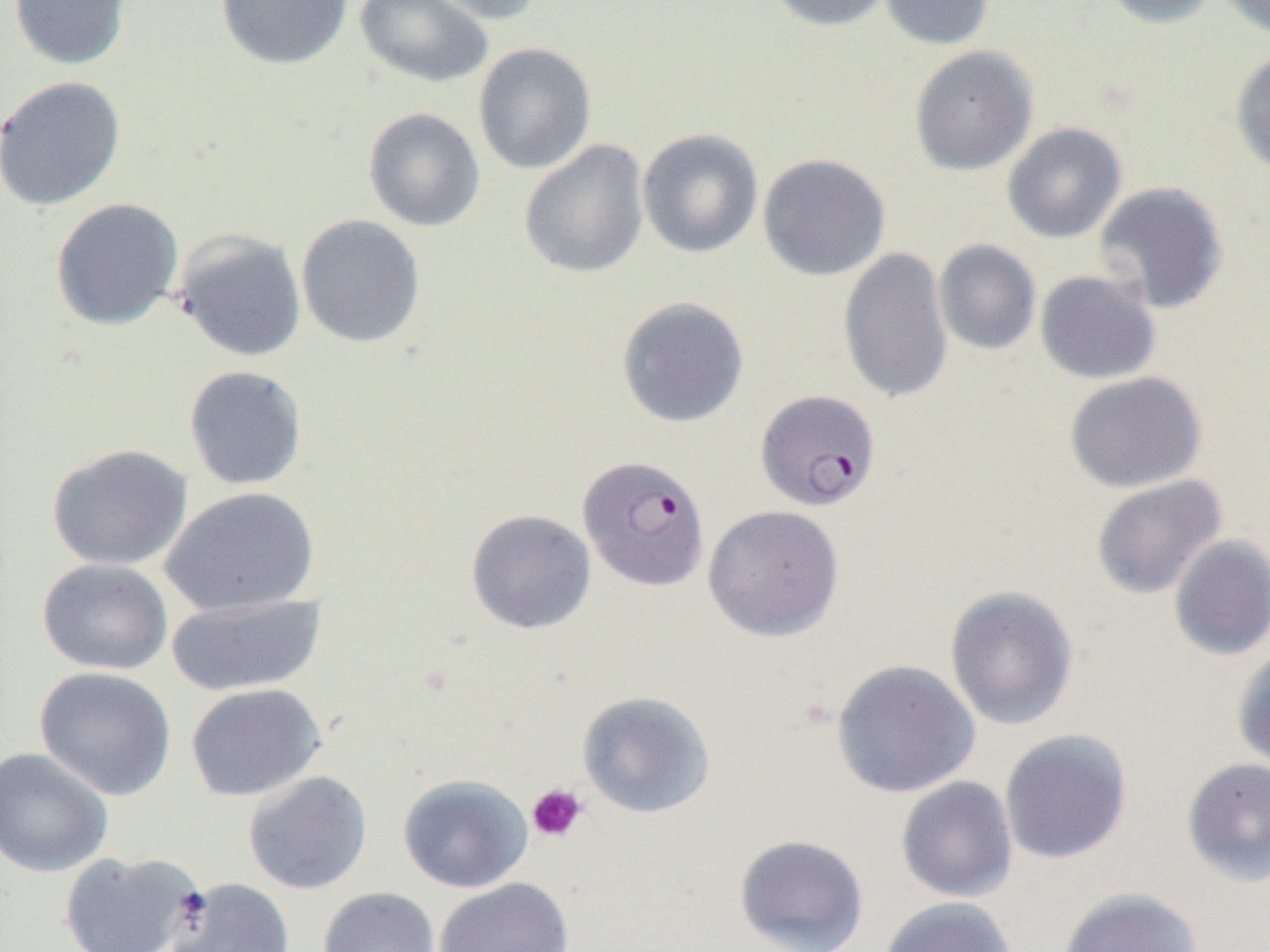

Approximate bounding boxes as named x1/y1/x2/y2 corners in pixels. Platelet locations: (x1=526, y1=784, x2=587, y2=842). Plasmodium falciparum-infected red blood cell locations: (x1=757, y1=391, x2=882, y2=513), (x1=577, y1=454, x2=711, y2=591). Uninfected red blood cell locations: (x1=7, y1=0, x2=132, y2=71), (x1=215, y1=0, x2=353, y2=70), (x1=354, y1=0, x2=494, y2=88), (x1=416, y1=0, x2=544, y2=25), (x1=766, y1=0, x2=895, y2=32), (x1=879, y1=0, x2=995, y2=50), (x1=1099, y1=0, x2=1223, y2=29), (x1=1216, y1=0, x2=1270, y2=38), (x1=473, y1=42, x2=597, y2=175), (x1=909, y1=45, x2=1038, y2=176), (x1=1230, y1=47, x2=1270, y2=180), (x1=0, y1=75, x2=126, y2=212), (x1=362, y1=107, x2=485, y2=233), (x1=1002, y1=122, x2=1126, y2=244), (x1=637, y1=128, x2=764, y2=258), (x1=518, y1=140, x2=649, y2=279), (x1=757, y1=153, x2=891, y2=281), (x1=1093, y1=181, x2=1230, y2=314), (x1=49, y1=198, x2=184, y2=331), (x1=295, y1=214, x2=426, y2=349), (x1=174, y1=229, x2=306, y2=362), (x1=934, y1=239, x2=1041, y2=355), (x1=837, y1=247, x2=954, y2=405), (x1=1035, y1=270, x2=1161, y2=384), (x1=616, y1=296, x2=750, y2=429), (x1=184, y1=365, x2=307, y2=491), (x1=1064, y1=371, x2=1207, y2=494), (x1=46, y1=444, x2=193, y2=571), (x1=1090, y1=474, x2=1228, y2=599), (x1=160, y1=486, x2=319, y2=616), (x1=703, y1=504, x2=845, y2=641), (x1=465, y1=508, x2=596, y2=635), (x1=1168, y1=535, x2=1270, y2=661), (x1=37, y1=558, x2=173, y2=675), (x1=944, y1=585, x2=1079, y2=730), (x1=165, y1=593, x2=327, y2=696), (x1=1231, y1=648, x2=1270, y2=775), (x1=831, y1=659, x2=981, y2=798), (x1=34, y1=666, x2=176, y2=800), (x1=186, y1=683, x2=326, y2=801), (x1=576, y1=691, x2=716, y2=819), (x1=998, y1=729, x2=1132, y2=865), (x1=0, y1=746, x2=114, y2=877), (x1=1182, y1=757, x2=1270, y2=887), (x1=243, y1=770, x2=372, y2=895), (x1=397, y1=774, x2=532, y2=893), (x1=895, y1=776, x2=1018, y2=903), (x1=734, y1=834, x2=869, y2=952), (x1=57, y1=850, x2=205, y2=952), (x1=165, y1=877, x2=295, y2=952), (x1=434, y1=877, x2=574, y2=952), (x1=318, y1=886, x2=440, y2=952), (x1=1058, y1=886, x2=1204, y2=952), (x1=878, y1=896, x2=1018, y2=952). Slide-level diagnosis: Plasmodium falciparum. Thin blood smear. Captured at 1000x magnification. Single field of view. Image is 1270×952 pixels. Optical microscopy.